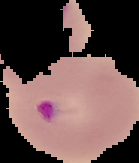

From a thin blood film. Image is 139×163 pixels. Malaria status: parasitized. The area outside the segmented cell region is set to black.